Assess the morphology of the erythrocytes.
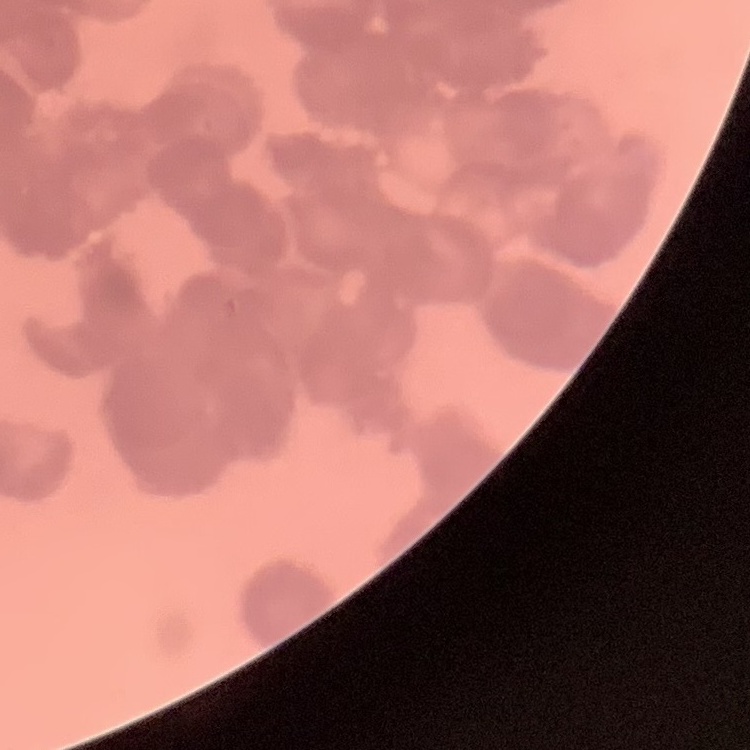

They show rouleaux formation.

Thin blood smear. One tile cut from a larger photomicrograph. Stained with either Field's or Giemsa.